State the blood parasite species.
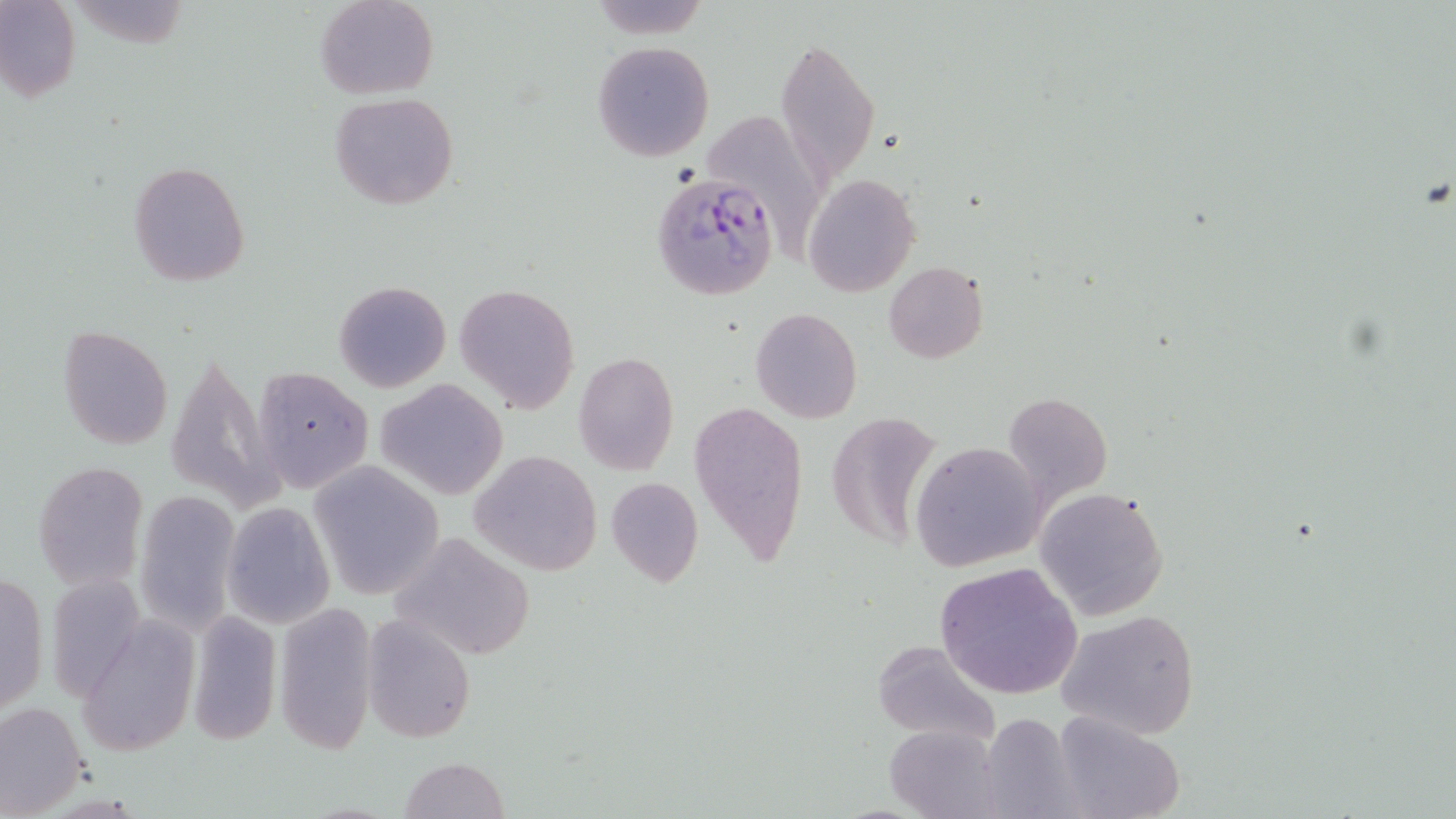

Plasmodium falciparum.

uninfected_red_blood_cell_locations: 'approximate bounding boxes as (x1,y1)-(x2,y2) corner pairs in pixels: (0,0)-(80,101), (315,0)-(437,99), (586,0)-(708,36), (775,36)-(881,185), (592,42)-(715,162), (330,93)-(459,209), (711,110)-(823,267), (128,161)-(250,285), (804,175)-(920,297), (884,262)-(988,363), (334,279)-(452,393), (455,282)-(580,413), (751,308)-(863,424), (58,326)-(173,449), (163,346)-(283,514), (573,352)-(679,475), (251,364)-(373,495), (376,378)-(509,500), (1003,390)-(1113,509), (688,397)-(809,565), (826,410)-(942,553), (909,442)-(1047,570), (469,450)-(604,576), (307,460)-(444,600), (35,461)-(148,591), (605,476)-(705,589), (1034,484)-(1171,621), (134,491)-(240,634), (222,502)-(335,628), (388,531)-(536,663), (367,556)-(509,725), (935,562)-(1084,702), (1,570)-(48,717), (47,575)-(144,704), (272,601)-(379,757), (187,607)-(286,748), (1057,608)-(1202,739), (361,614)-(474,746), (75,618)-(199,758), (870,639)-(1001,744), (0,702)-(87,815), (981,711)-(1079,817), (1051,711)-(1187,819), (885,724)-(1002,819), (397,756)-(508,819)'
magnification: 1000x
preparation: thin blood smear
field_of_view: one of a larger specimen
plasmodium_falciparum_infected_red_blood_cell_locations: 'approximate bounding boxes as (x1,y1)-(x2,y2) corner pairs in pixels: (651,172)-(779,300)'
modality: optical microscopy
image_size: 1456×819 pixels
stain: May-Grünwald-Giemsa